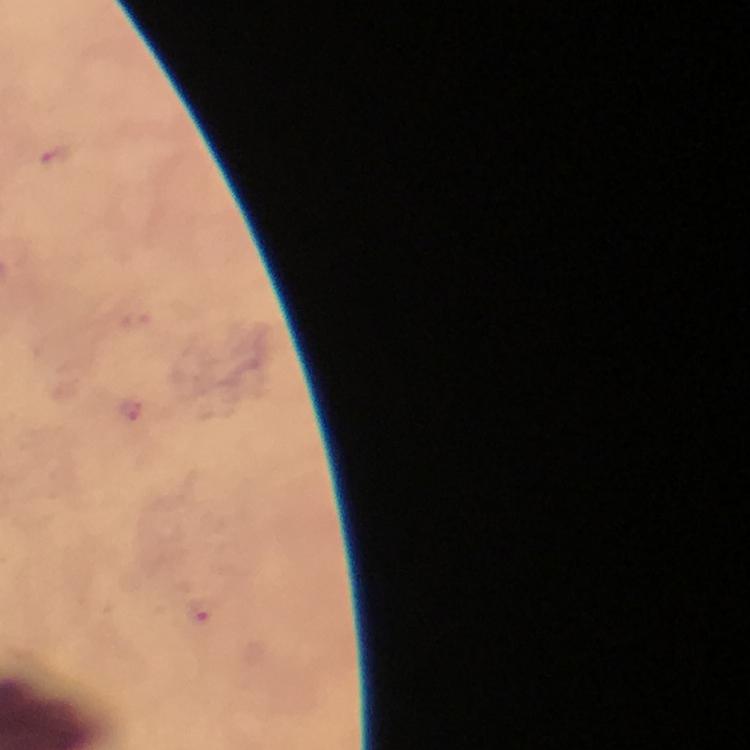

Approximate centers as (x, y) in pixels.
Summary:
  - Malaria parasite locations: (53, 156), (200, 612)
  - Immersion oil: applied
  - Capture: smartphone photograph through a microscope
  - Stain: Giemsa
  - Image size: 750×750 pixels
  - Context: from a malaria diagnostic workup
  - Magnification: 100x
  - Preparation: thick blood smear
  - Cropped from: one field of view